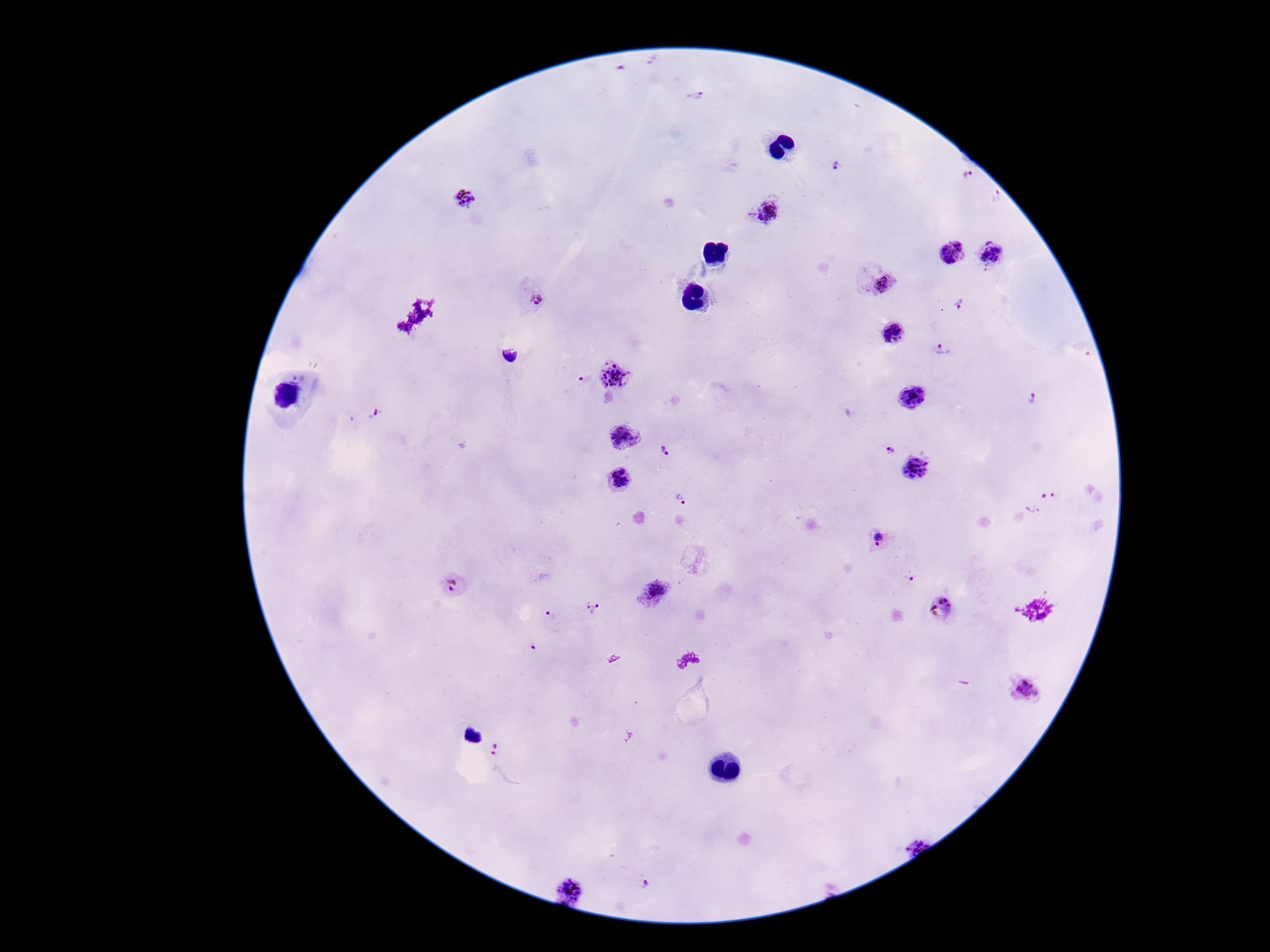

Approximate centers as (x, y) in pixels. Plasmodium parasite locations: (695, 96), (839, 167), (968, 176), (465, 200), (767, 210), (952, 256), (991, 257), (877, 281), (532, 296), (959, 305), (894, 333), (942, 350), (615, 374), (585, 379), (913, 398), (1033, 398), (624, 437), (890, 450), (664, 452), (914, 469), (620, 478), (680, 500), (880, 540), (911, 579), (454, 586), (654, 591), (941, 607), (595, 610), (550, 616), (1025, 691), (496, 750), (644, 884), (572, 887). Photographed through the microscope eyepiece with a smartphone camera. Thick peripheral-blood smear. 100x magnification. Patient malaria status: positive. Single field of view. Giemsa-stained preparation. Image is 1270×952 pixels.